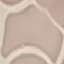
malaria status = uninfected
preparation = thin smear
capture = smartphone camera at the microscope eyepiece
image type = cell patch, automatically extracted from a larger field of view and resized to 64 × 64 pixels
stain = Giemsa